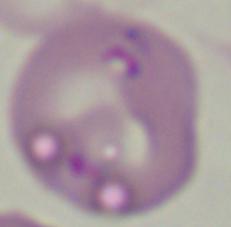
modality: photomicrograph
identification: Babesia
magnification: 1000x